Locate and identify every blood parasite.
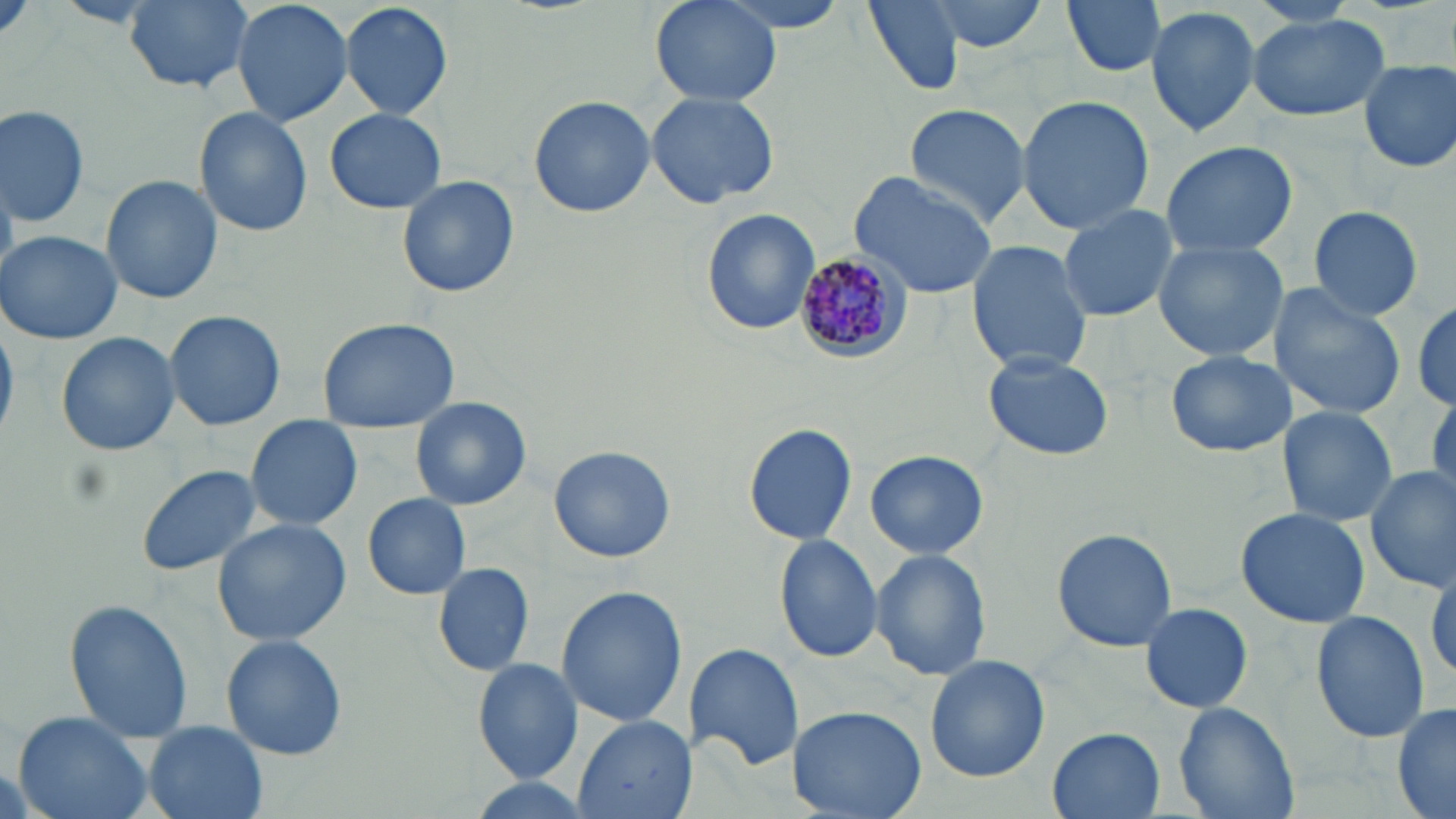
Approximate bounding boxes as (x1,y1)-(x2,y2) corner pairs in pixels.
Plasmodium malariae-infected red blood cells: (789,251)-(910,363).
No Plasmodium falciparum, Plasmodium ovale, Plasmodium vivax, Babesia divergens, or Trypanosoma brucei observed.

slide-level diagnosis = Plasmodium malariae
magnification = 1000x
preparation = thin blood film
stain = May-Grünwald-Giemsa
uninfected red blood cell locations = approximate bounding boxes as (x1,y1)-(x2,y2) corner pairs in pixels: (122,0)-(256,94), (230,0)-(355,128), (338,0)-(453,121), (650,0)-(781,109), (861,0)-(967,95), (924,0)-(1052,51), (1061,0)-(1169,80), (55,1)-(159,29), (1145,4)-(1264,139), (1246,13)-(1390,122), (1357,59)-(1455,174), (646,89)-(780,209), (528,94)-(655,218), (1016,95)-(1156,235), (902,103)-(1033,227), (0,104)-(91,229), (194,106)-(313,237), (326,108)-(445,214), (1158,139)-(1300,260), (846,171)-(998,299), (101,174)-(223,304), (397,174)-(520,298), (1308,206)-(1424,320), (1057,207)-(1179,322), (700,208)-(820,337), (0,231)-(124,344), (965,240)-(1094,377), (1154,240)-(1288,361), (1269,285)-(1404,420), (1411,293)-(1456,415), (163,310)-(286,430), (315,317)-(460,431), (56,332)-(180,458), (983,347)-(1113,458), (1166,349)-(1295,456), (410,398)-(532,510), (1276,405)-(1397,529), (245,414)-(364,532), (744,422)-(858,547), (549,445)-(677,563), (866,449)-(988,561), (136,465)-(262,577), (1365,466)-(1455,591), (361,492)-(472,599), (1236,506)-(1370,628), (212,516)-(355,646), (1051,528)-(1176,651), (773,534)-(884,664), (870,547)-(992,683), (1427,556)-(1456,685), (431,560)-(536,676), (555,586)-(687,730), (65,600)-(193,740), (1139,601)-(1253,713), (1311,610)-(1429,743), (221,634)-(348,760), (685,644)-(804,771), (924,654)-(1052,781), (472,658)-(585,783), (1173,701)-(1298,819), (1391,703)-(1455,819), (787,704)-(928,819), (10,710)-(156,819), (571,715)-(693,819), (145,722)-(267,819), (1046,728)-(1167,818)
field of view = single
image size = 1456×819 pixels
modality = light microscopy